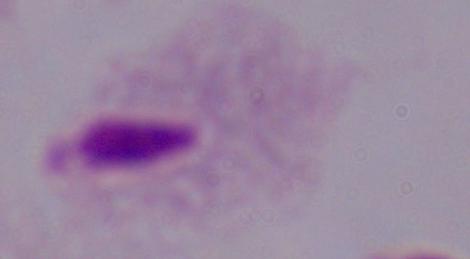

1000x magnification. A trichomonad is seen. Photomicrograph.